Comment on the morphology of the erythrocytes.
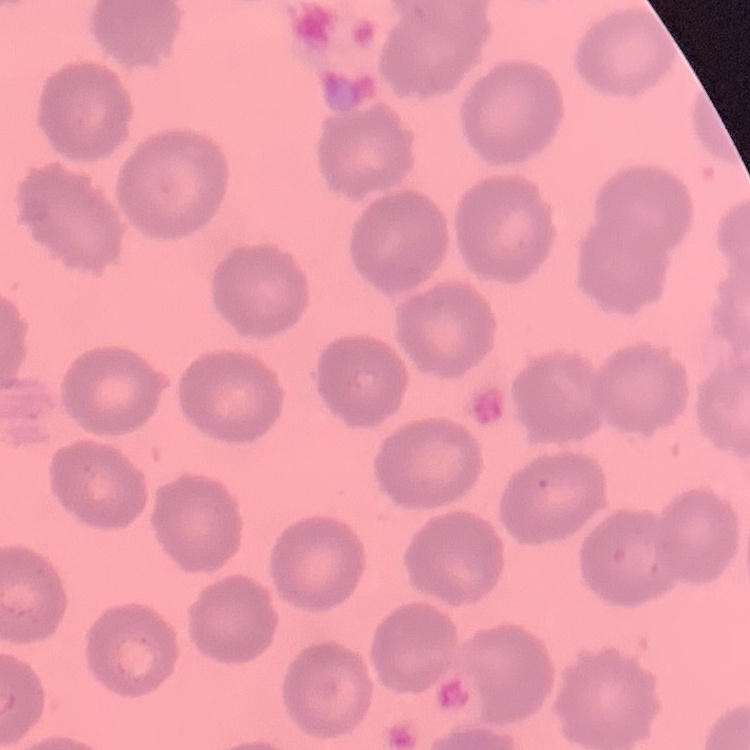
No rouleaux formation.

image type = one tile cut from a larger photomicrograph
preparation = thin blood smear
stain = Field's or Giemsa